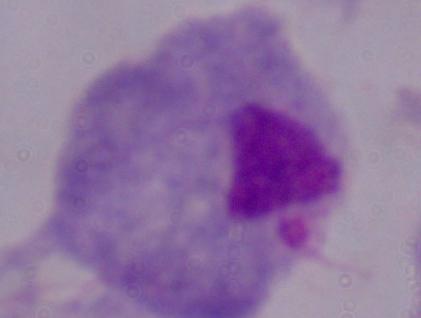

Summary:
  - Identification: trichomonad
  - Modality: micrograph
  - Magnification: 1000x